State which cell type is depicted.
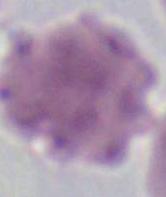

An erythrocyte.

modality = photomicrograph
magnification = 1000x